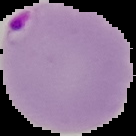
preparation = thin blood smear
image size = 136×136 pixels
result = malaria parasites detected
image type = segmented cell region on a black background